State the blood parasite species.
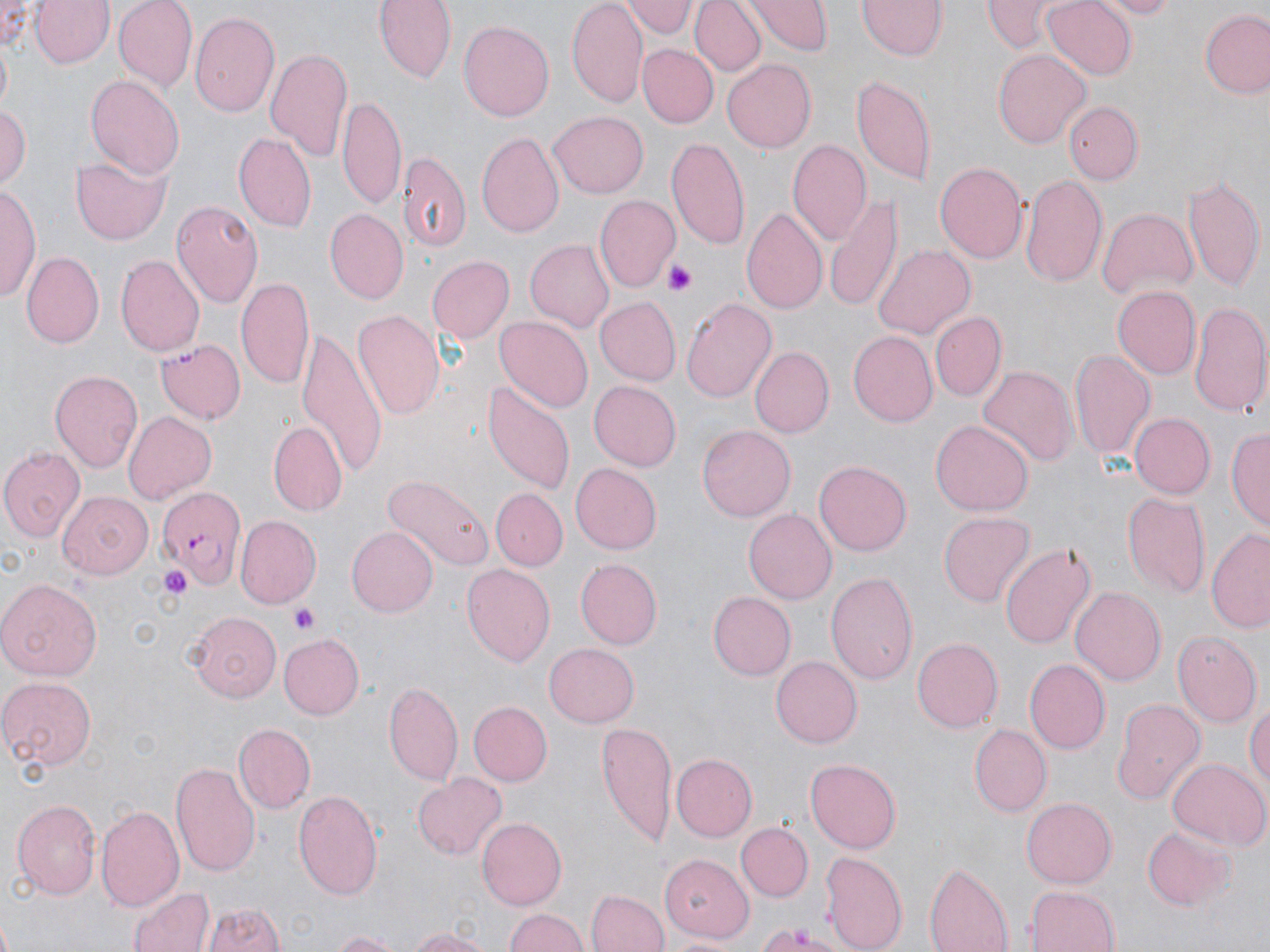
Plasmodium falciparum.

Approximate bounding boxes as (x1, y1, x2, y2) in pixels. Uninfected red blood cell locations: (0, 0, 37, 50), (377, 0, 454, 82), (621, 0, 696, 39), (689, 0, 763, 76), (749, 0, 830, 53), (860, 0, 945, 60), (982, 0, 1065, 50), (1041, 0, 1136, 80), (1088, 0, 1183, 17), (30, 1, 113, 69), (113, 1, 197, 93), (568, 2, 649, 108), (1200, 10, 1270, 98), (191, 12, 281, 118), (459, 19, 556, 121), (638, 45, 716, 128), (268, 47, 354, 166), (993, 49, 1089, 147), (722, 58, 816, 153), (84, 72, 184, 178), (852, 75, 937, 184), (338, 94, 406, 207), (1063, 100, 1144, 186), (0, 103, 30, 188), (547, 111, 648, 198), (476, 132, 563, 240), (234, 134, 316, 234), (667, 138, 750, 251), (788, 140, 870, 246), (400, 153, 471, 255), (70, 158, 168, 244), (934, 162, 1027, 265), (1021, 172, 1108, 289), (1184, 172, 1264, 291), (0, 184, 40, 300), (595, 194, 678, 290), (825, 194, 904, 313), (169, 198, 261, 307), (742, 207, 829, 317), (1097, 207, 1198, 300), (325, 209, 409, 303), (522, 241, 616, 331), (874, 245, 974, 339), (22, 249, 104, 346), (116, 255, 204, 357), (424, 255, 514, 344), (237, 277, 316, 391), (1112, 288, 1199, 378), (681, 295, 776, 405), (595, 298, 681, 385), (1191, 301, 1270, 419), (353, 309, 446, 419), (932, 312, 1005, 401), (495, 315, 593, 415), (296, 328, 387, 478), (849, 332, 937, 425), (156, 338, 245, 424), (749, 346, 834, 437), (1069, 349, 1153, 461), (978, 366, 1077, 468), (52, 369, 145, 473), (480, 379, 575, 496), (589, 381, 681, 470), (121, 411, 215, 504), (1129, 414, 1216, 498), (930, 420, 1033, 515), (268, 423, 348, 518), (698, 425, 796, 521), (1228, 428, 1270, 531), (0, 444, 84, 541), (815, 460, 912, 555), (571, 464, 661, 554), (383, 473, 493, 571), (492, 488, 567, 569), (1121, 490, 1211, 601), (57, 492, 152, 579), (744, 509, 836, 604), (938, 512, 1034, 607), (234, 517, 320, 611), (345, 526, 436, 616), (1207, 527, 1270, 633), (999, 541, 1095, 652), (575, 558, 662, 649), (461, 563, 556, 666), (827, 571, 919, 687), (0, 578, 102, 680), (1071, 586, 1166, 685), (708, 591, 795, 680), (183, 610, 281, 701), (1171, 630, 1260, 728), (279, 633, 365, 719), (913, 637, 1003, 732), (545, 643, 640, 727), (771, 657, 862, 747), (1026, 659, 1110, 755), (0, 676, 98, 774), (384, 682, 463, 786), (1109, 697, 1207, 805), (1246, 697, 1270, 794), (470, 701, 551, 785), (598, 722, 674, 846), (234, 724, 314, 812), (969, 724, 1050, 817), (671, 755, 756, 840), (805, 759, 901, 851), (1166, 759, 1267, 851), (171, 763, 260, 880), (412, 773, 506, 860), (294, 788, 385, 900), (1022, 797, 1117, 886), (12, 800, 100, 901), (96, 804, 184, 912), (476, 816, 566, 909), (737, 823, 812, 899), (1140, 825, 1231, 910), (820, 849, 908, 952), (659, 853, 755, 940), (924, 862, 1013, 952), (130, 886, 214, 952), (1024, 886, 1121, 952), (585, 889, 667, 952), (204, 904, 285, 952), (503, 908, 593, 952), (750, 921, 850, 950), (404, 925, 496, 952), (328, 929, 400, 952). Platelet locations: (665, 261, 697, 296), (155, 563, 195, 602), (291, 604, 320, 635). Plasmodium falciparum-infected red blood cell locations: (155, 486, 244, 587). May-Grünwald-Giemsa-stained preparation. Light microscopy. 1000x magnification. Image is 1270×952 pixels. Single field of view. Thin blood film.